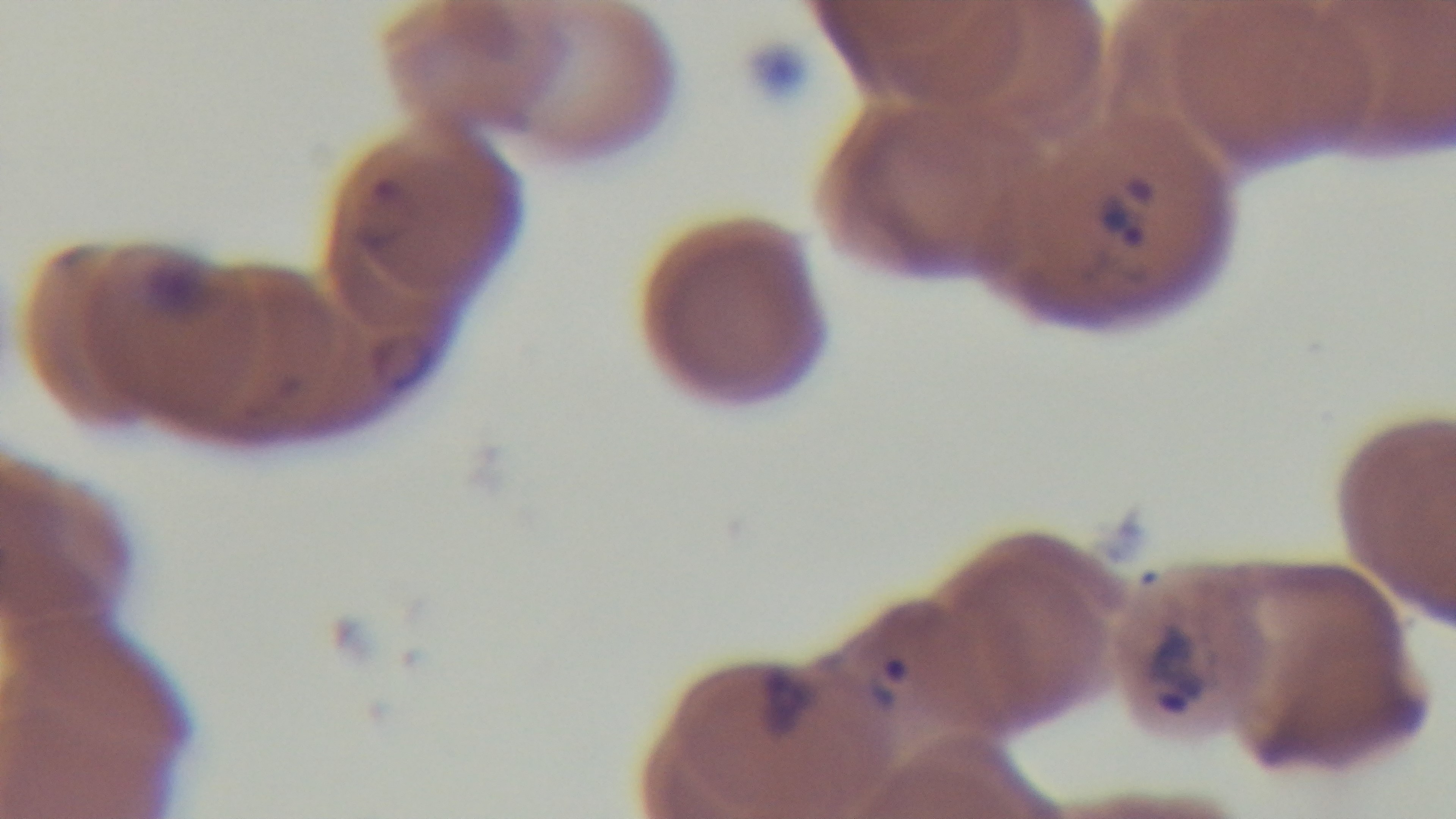
Oil-immersion objective, 100x. Malaria status: infected. One field from the slide. Photomicrograph. Giemsa stain. Mounted 4K digital camera. Preparation: thin smear.